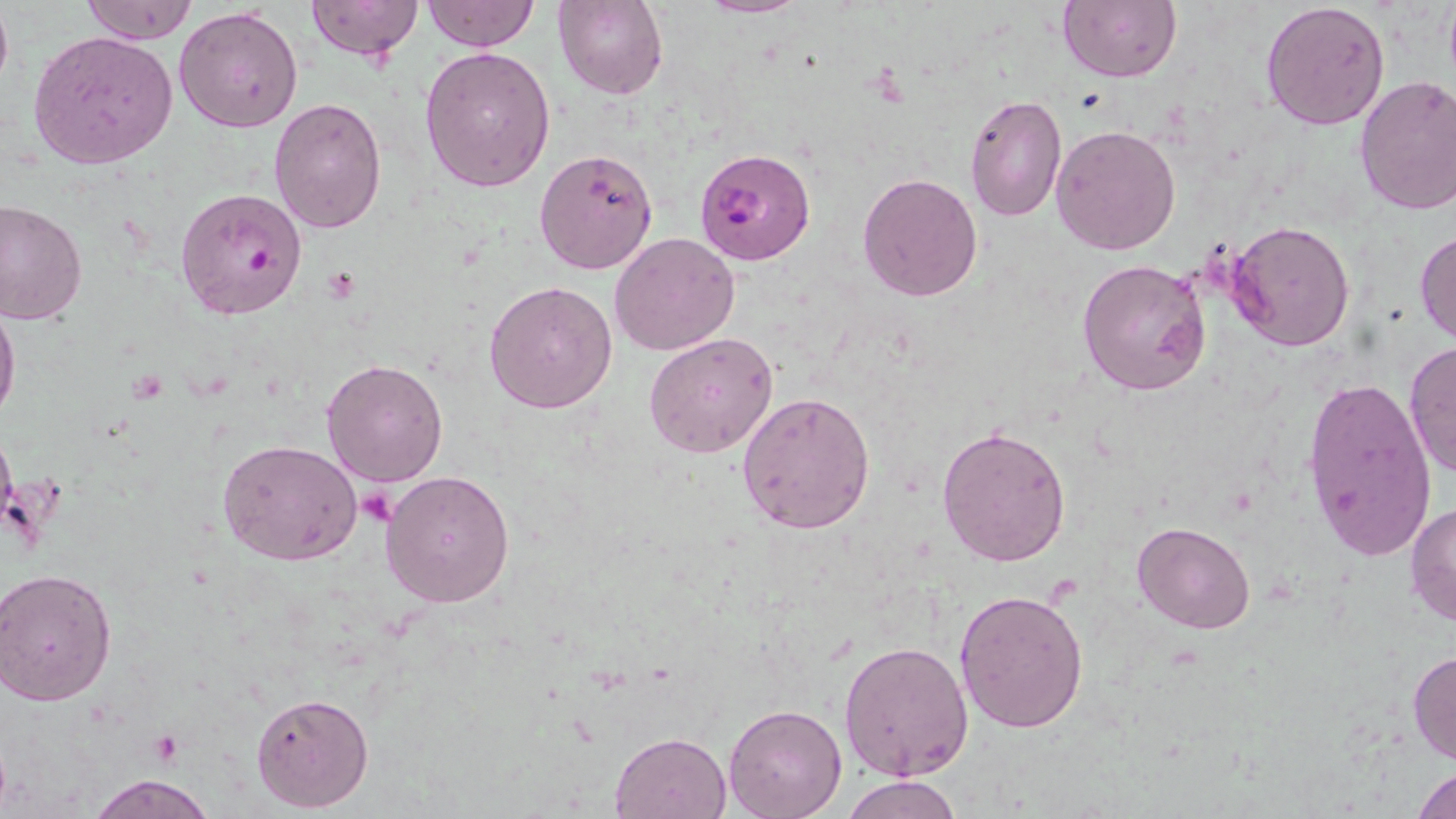

Summary:
  - Coordinate format: approximate bounding boxes as (x1, y1, x2, y2) in pixels
  - Platelet locations: (355, 488, 396, 525), (147, 729, 187, 768)
  - Plasmodium falciparum-infected red blood cell locations: (694, 147, 816, 263), (174, 187, 308, 320)
  - Uninfected red blood cell locations: (0, 0, 13, 100), (81, 0, 199, 44), (305, 0, 424, 61), (421, 0, 539, 52), (696, 0, 807, 18), (1058, 0, 1181, 83), (554, 1, 668, 100), (1261, 2, 1391, 132), (175, 5, 305, 133), (27, 31, 178, 168), (419, 47, 556, 192), (1354, 74, 1456, 216), (269, 95, 386, 233), (963, 95, 1067, 222), (1050, 124, 1181, 255), (534, 148, 658, 274), (857, 172, 983, 301), (0, 197, 87, 325), (1225, 219, 1357, 353), (1415, 227, 1456, 345), (611, 232, 740, 355), (1077, 258, 1210, 397), (485, 280, 617, 414), (1, 291, 21, 432), (644, 333, 779, 459), (1403, 340, 1456, 482), (321, 357, 450, 488), (1301, 376, 1438, 562), (736, 390, 877, 533), (937, 424, 1071, 566), (218, 439, 362, 565), (380, 471, 515, 610), (1406, 501, 1456, 626), (1133, 522, 1256, 634), (2, 568, 119, 706), (954, 587, 1089, 734), (838, 639, 973, 781), (1407, 648, 1456, 765), (250, 690, 376, 813), (724, 704, 848, 819), (610, 730, 731, 818), (1409, 762, 1456, 819), (88, 774, 217, 819), (841, 774, 961, 818)
  - Slide-level diagnosis: Plasmodium falciparum
  - Image size: 1456×819 pixels
  - Magnification: 1000x
  - Field of view: single
  - Modality: optical microscopy
  - Stain: May-Grünwald-Giemsa
  - Preparation: thin blood smear